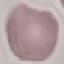
Summary:
  - Result: no malaria parasites seen
  - Stain: Giemsa
  - Image type: automatically extracted cell patch, resized to 64 × 64 pixels
  - Preparation: thin smear
  - Capture: smartphone through the microscope eyepiece